Report the malaria status of this cell.
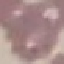

Uninfected.

Summary:
  - Image type: automatically extracted cell patch, resized to 64 × 64 pixels
  - Preparation: thin blood film
  - Capture: smartphone camera at the microscope eyepiece
  - Stain: Giemsa